State which parasite is depicted.
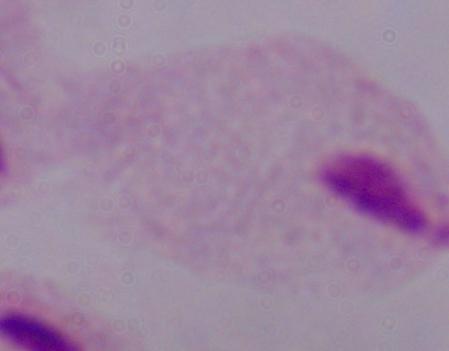
This is a trichomonad.

Summary:
  - Modality: micrograph
  - Magnification: 1000x